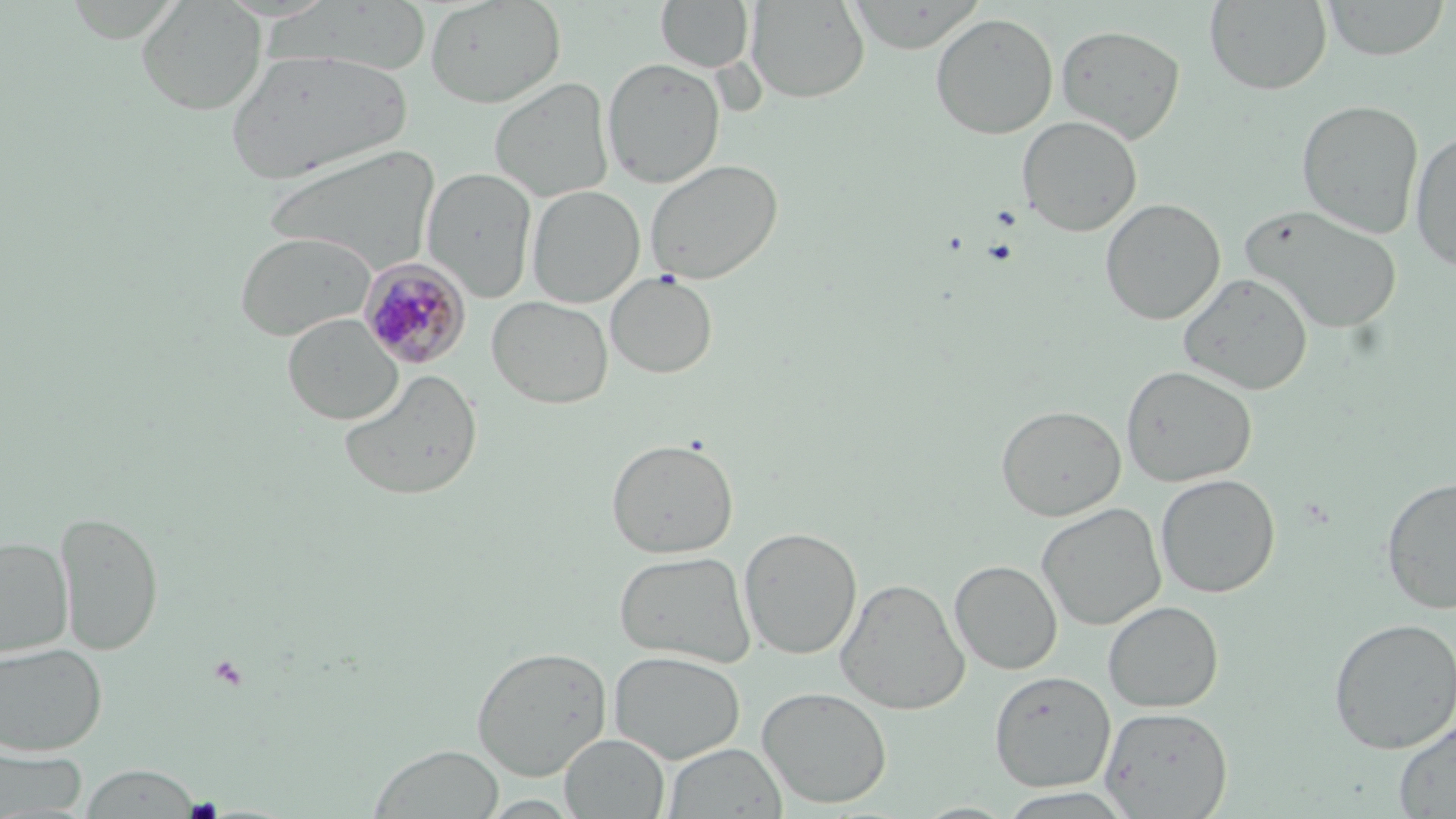

Plasmodium malariae-infected red blood cell locations = approximate bounding boxes as (x1,y1)-(x2,y2) corner pairs in pixels: (358,257)-(471,369)
slide-level diagnosis = Plasmodium malariae
platelet locations = approximate bounding boxes as (x1,y1)-(x2,y2) corner pairs in pixels: (208,657)-(250,691)
stain = May-Grünwald-Giemsa
magnification = 1000x
field of view = one of a larger specimen
uninfected red blood cell locations = approximate bounding boxes as (x1,y1)-(x2,y2) corner pairs in pixels: (136,0)-(267,115), (424,0)-(566,109), (746,0)-(870,103), (1205,0)-(1332,95), (1321,0)-(1450,60), (656,1)-(754,72), (845,2)-(984,53), (930,13)-(1058,139), (1056,24)-(1185,143), (225,46)-(413,183), (602,57)-(726,188), (489,77)-(615,203), (1297,99)-(1423,239), (1017,115)-(1142,236), (1410,131)-(1456,271), (263,144)-(441,277), (645,158)-(784,285), (422,166)-(537,304), (526,185)-(645,308), (1101,198)-(1225,325), (1240,204)-(1402,334), (234,230)-(377,342), (1180,271)-(1313,395), (605,272)-(717,378), (487,295)-(613,409), (282,313)-(404,425), (1120,365)-(1258,487), (339,369)-(483,500), (996,404)-(1126,521), (606,437)-(739,559), (1155,474)-(1280,598), (1380,476)-(1456,615), (1036,502)-(1166,630), (55,510)-(163,656), (738,526)-(862,660), (0,535)-(73,658), (614,550)-(756,668), (949,560)-(1062,675), (835,577)-(969,715), (1103,600)-(1223,712), (1328,617)-(1456,754), (0,642)-(107,756), (471,645)-(612,780), (608,650)-(745,764), (990,671)-(1115,791), (757,686)-(893,808), (1100,706)-(1233,818), (1393,720)-(1456,817), (560,733)-(670,818), (0,743)-(89,816), (662,743)-(787,818), (368,744)-(505,819), (79,764)-(202,817)
preparation = thin blood smear
modality = optical microscopy
image size = 1456×819 pixels